Locate and identify every blood parasite.
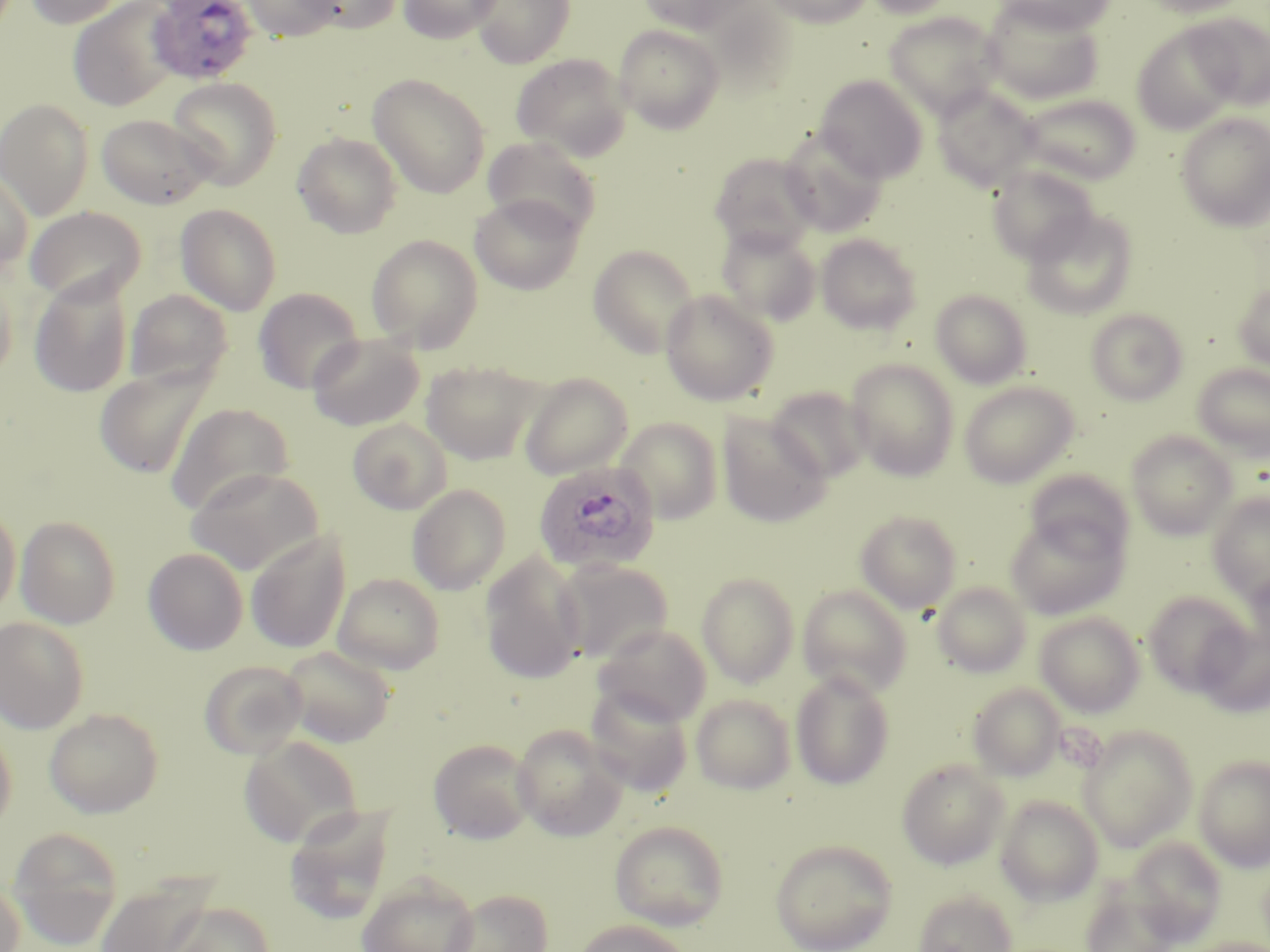
Approximate bounding boxes as named x1/y1/x2/y2 corners in pixels.
Plasmodium ovale-infected red blood cells: (x1=145, y1=0, x2=258, y2=84), (x1=532, y1=460, x2=660, y2=575).
No Plasmodium falciparum, Plasmodium malariae, Plasmodium vivax, Babesia divergens, or Trypanosoma brucei observed.

Summary:
  - Uninfected red blood cell locations: (x1=25, y1=0, x2=128, y2=28), (x1=241, y1=0, x2=340, y2=41), (x1=301, y1=0, x2=401, y2=34), (x1=398, y1=0, x2=502, y2=43), (x1=471, y1=0, x2=575, y2=68), (x1=639, y1=0, x2=756, y2=34), (x1=765, y1=0, x2=873, y2=28), (x1=863, y1=0, x2=959, y2=19), (x1=997, y1=0, x2=1118, y2=36), (x1=1139, y1=0, x2=1254, y2=17), (x1=67, y1=1, x2=180, y2=111), (x1=982, y1=1, x2=1105, y2=105), (x1=882, y1=11, x2=1004, y2=119), (x1=1187, y1=13, x2=1270, y2=110), (x1=614, y1=24, x2=725, y2=134), (x1=1132, y1=24, x2=1242, y2=134), (x1=511, y1=52, x2=633, y2=161), (x1=367, y1=73, x2=491, y2=199), (x1=815, y1=75, x2=928, y2=183), (x1=167, y1=76, x2=283, y2=189), (x1=932, y1=85, x2=1040, y2=191), (x1=1019, y1=93, x2=1141, y2=185), (x1=0, y1=98, x2=94, y2=219), (x1=96, y1=113, x2=216, y2=210), (x1=1176, y1=113, x2=1270, y2=232), (x1=779, y1=129, x2=888, y2=236), (x1=292, y1=131, x2=403, y2=239), (x1=482, y1=136, x2=602, y2=239), (x1=709, y1=151, x2=819, y2=253), (x1=987, y1=164, x2=1098, y2=264), (x1=0, y1=166, x2=34, y2=274), (x1=469, y1=194, x2=584, y2=295), (x1=175, y1=203, x2=282, y2=315), (x1=24, y1=206, x2=147, y2=305), (x1=1023, y1=209, x2=1138, y2=319), (x1=716, y1=224, x2=820, y2=326), (x1=366, y1=233, x2=483, y2=352), (x1=816, y1=234, x2=922, y2=334), (x1=588, y1=244, x2=699, y2=358), (x1=0, y1=255, x2=21, y2=379), (x1=28, y1=273, x2=134, y2=398), (x1=1233, y1=281, x2=1270, y2=371), (x1=253, y1=287, x2=364, y2=394), (x1=124, y1=289, x2=233, y2=390), (x1=660, y1=289, x2=779, y2=406), (x1=931, y1=289, x2=1032, y2=388), (x1=1085, y1=308, x2=1188, y2=405), (x1=307, y1=334, x2=424, y2=430), (x1=845, y1=358, x2=960, y2=481), (x1=421, y1=360, x2=539, y2=464), (x1=94, y1=363, x2=214, y2=479), (x1=1192, y1=363, x2=1270, y2=460), (x1=518, y1=373, x2=632, y2=478), (x1=959, y1=380, x2=1078, y2=488), (x1=766, y1=386, x2=871, y2=484), (x1=165, y1=402, x2=293, y2=516), (x1=717, y1=414, x2=832, y2=528), (x1=616, y1=417, x2=723, y2=524), (x1=348, y1=418, x2=452, y2=514), (x1=1127, y1=431, x2=1236, y2=540), (x1=185, y1=465, x2=324, y2=574), (x1=1024, y1=469, x2=1133, y2=561), (x1=407, y1=484, x2=511, y2=595), (x1=1207, y1=492, x2=1270, y2=604), (x1=0, y1=503, x2=21, y2=617), (x1=855, y1=509, x2=962, y2=613), (x1=1005, y1=512, x2=1129, y2=619), (x1=14, y1=515, x2=121, y2=629), (x1=246, y1=532, x2=350, y2=654), (x1=143, y1=547, x2=248, y2=655), (x1=479, y1=553, x2=587, y2=684), (x1=554, y1=560, x2=673, y2=664), (x1=1245, y1=568, x2=1270, y2=657), (x1=696, y1=571, x2=800, y2=687), (x1=332, y1=572, x2=445, y2=674), (x1=932, y1=581, x2=1031, y2=677), (x1=797, y1=584, x2=913, y2=697), (x1=1143, y1=591, x2=1251, y2=697), (x1=1035, y1=612, x2=1145, y2=717), (x1=0, y1=616, x2=90, y2=733), (x1=1195, y1=621, x2=1270, y2=718), (x1=594, y1=623, x2=712, y2=726), (x1=281, y1=645, x2=396, y2=747), (x1=199, y1=659, x2=308, y2=759), (x1=790, y1=669, x2=895, y2=790), (x1=967, y1=683, x2=1066, y2=781), (x1=585, y1=685, x2=694, y2=797), (x1=691, y1=693, x2=796, y2=794), (x1=44, y1=707, x2=164, y2=818), (x1=0, y1=720, x2=17, y2=837), (x1=511, y1=724, x2=628, y2=841), (x1=1077, y1=725, x2=1198, y2=852), (x1=239, y1=735, x2=363, y2=848), (x1=428, y1=738, x2=536, y2=844), (x1=1194, y1=754, x2=1270, y2=872), (x1=896, y1=759, x2=1009, y2=870), (x1=995, y1=795, x2=1104, y2=906), (x1=284, y1=805, x2=398, y2=925), (x1=609, y1=820, x2=730, y2=930), (x1=6, y1=826, x2=125, y2=948), (x1=1126, y1=836, x2=1226, y2=944), (x1=770, y1=839, x2=897, y2=952), (x1=355, y1=873, x2=481, y2=952), (x1=0, y1=875, x2=26, y2=952), (x1=93, y1=876, x2=218, y2=952), (x1=1080, y1=879, x2=1182, y2=952), (x1=443, y1=888, x2=553, y2=952), (x1=912, y1=889, x2=1018, y2=952), (x1=163, y1=901, x2=275, y2=952), (x1=573, y1=919, x2=694, y2=952), (x1=1180, y1=937, x2=1270, y2=952)
  - Slide-level diagnosis: Plasmodium ovale
  - Stain: May-Grünwald-Giemsa
  - Field of view: one of a larger specimen
  - Preparation: thin blood film
  - Image size: 1270×952 pixels
  - Magnification: 1000x
  - Modality: optical microscopy